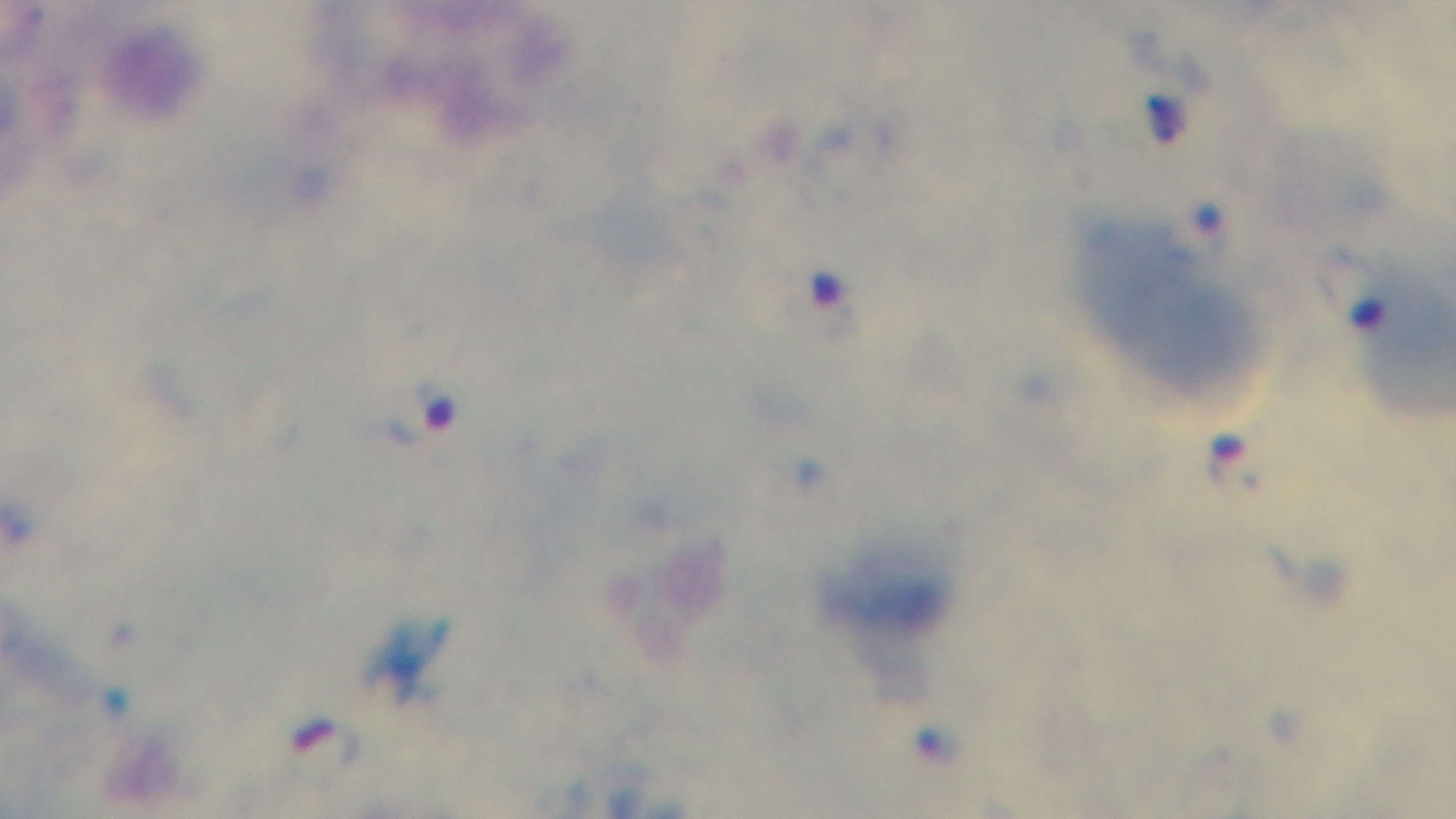

Captured with a mounted 4K digital camera. Preparation: thick smear. Giemsa stain. One field from the slide. Malaria status: infected. Oil-immersion objective, 100x. Light microscopy.